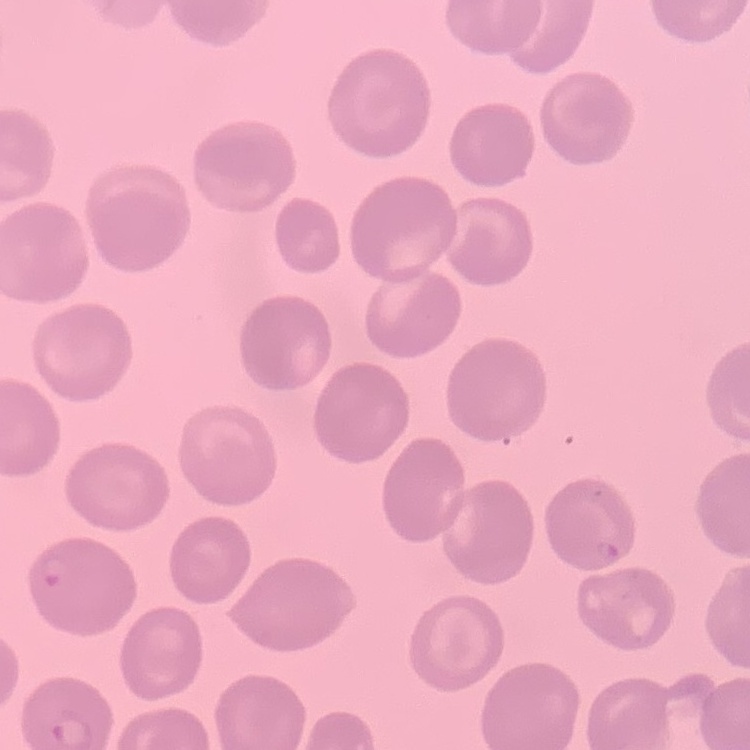

red_blood_cell_morphology: no rouleaux formation
image_type: square crop of a larger photomicrograph
preparation: thin blood smear
stain: Field's or Giemsa